Assess this cell for malaria.
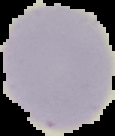

It is uninfected.

{
  "image_type": "segmented cell region with the area outside set to black",
  "image_size": "115×136 pixels",
  "preparation": "thin blood film"
}